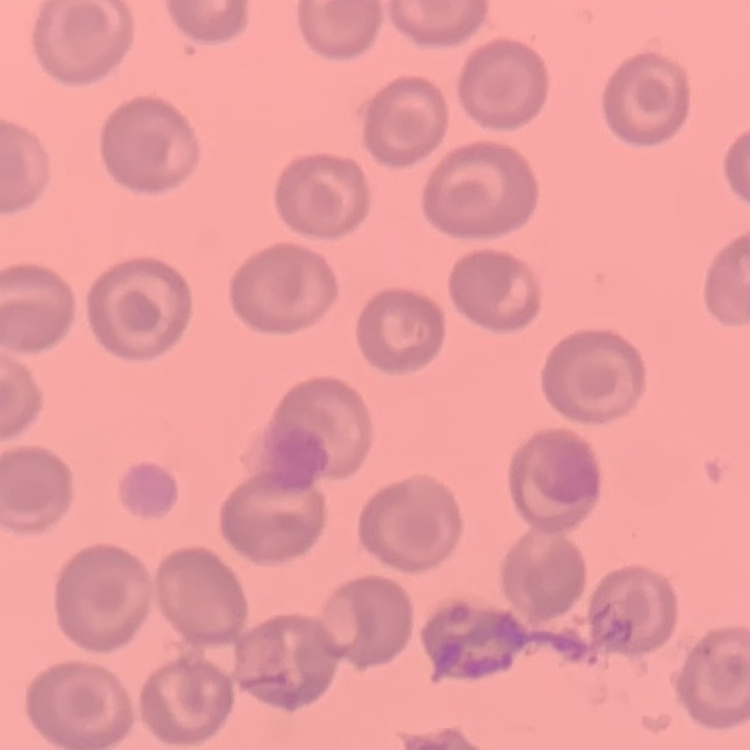 The red blood cells show no rouleaux formation. Square crop of a larger photomicrograph. Stained with either Field's or Giemsa. Thin blood smear.